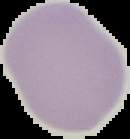
Summary:
  - Result: no Plasmodium parasites seen
  - Image size: 130×139 pixels
  - Preparation: thin blood smear
  - Image type: cell region segmented out of the field of view; surrounding area masked to black